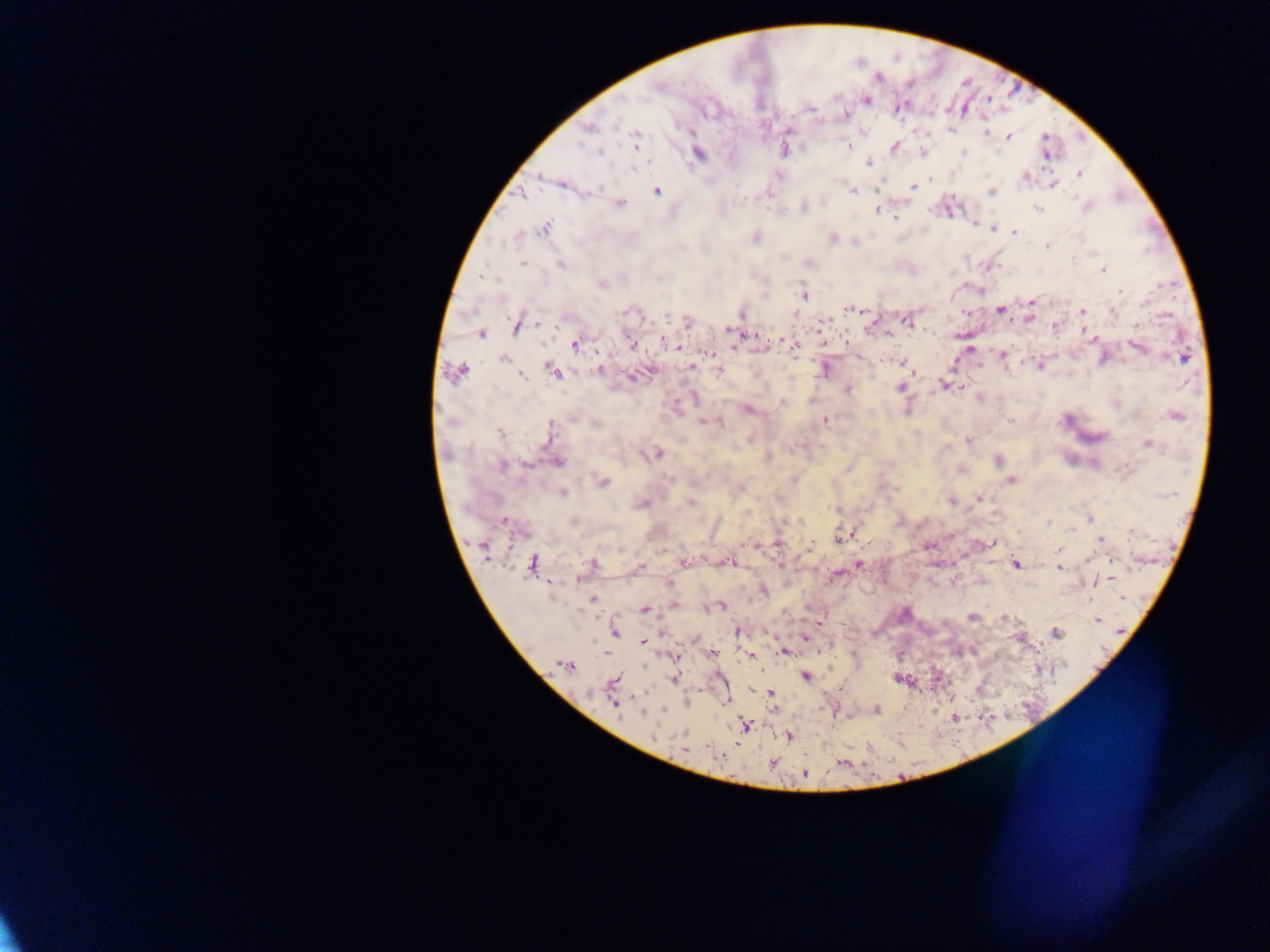 Approximate centers as x y in pixels. Plasmodium parasite locations: 989 99; 868 100; 964 108; 810 110; 898 110; 845 115; 819 122; 613 124; 590 129; 950 133; 987 133; 635 134; 1008 137; 848 146; 895 146; 636 147; 965 153; 602 154; 924 155; 1046 155; 867 162; 632 170; 1026 176; 1080 176; 561 184; 912 186; 1054 186; 597 187; 657 190; 852 192; 993 193; 523 194; 621 203; 805 208; 1088 209; 1039 210; 876 211; 944 211; 896 218; 546 226; 993 228; 1015 232; 1077 236; 519 237; 832 238; 854 242; 1049 247; 1092 250; 1074 258; 521 265; 560 265; 1107 267; 1103 271; 1120 292; 803 295; 1032 298; 849 307; 999 310; 1082 312; 1114 312; 666 315; 1029 319; 908 322; 1139 325; 516 326; 821 327; 727 331; 481 334; 753 335; 659 336; 782 338; 663 340; 843 343; 632 345; 576 346; 677 346; 796 346; 1138 348; 707 353; 1004 354; 1183 358; 503 360; 955 360; 900 363; 1041 367; 549 368; 691 368; 718 369; 462 370; 599 370; 824 370; 651 371; 556 373; 522 377; 630 377; 944 382; 900 388; 847 390; 980 397; 782 402; 748 411; 1179 416; 700 421; 826 421; 1010 421; 596 424; 551 428; 500 433; 749 439; 968 440; 1148 444; 945 447; 658 454; 649 455; 996 460; 557 462; 1074 462; 504 467; 960 471; 1012 480; 605 483; 563 492; 979 496; 950 502; 691 503; 835 509; 1090 518; 503 521; 574 521; 1049 522; 1070 531; 1130 532; 839 538; 1101 540; 991 542; 1057 548; 622 549; 1091 557; 684 562; 731 562; 592 563; 778 563; 860 564; 1016 564; 530 565; 641 566; 1059 567; 784 568; 837 574; 1112 577; 1095 582; 550 583; 763 592; 593 599; 1121 600; 721 606; 644 611; 972 616; 1004 619; 818 620; 1097 620; 737 631; 615 632; 1056 632; 663 633; 803 638; 642 643; 783 652; 712 653; 750 656; 804 677; 892 678; 674 679; 770 693; 614 705; 877 710; 663 711; 641 715; 789 735; 707 750; 718 754; 772 765; 805 773. Mobile-phone photograph taken through the microscope. Collected in Ghana. Thick blood smear. Image is 1270×952 pixels. Single field of view.